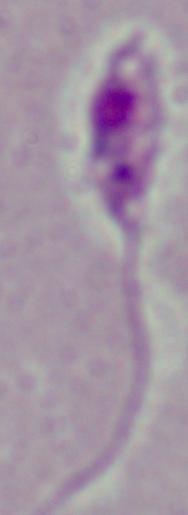

magnification: 1000x
identification: Leishmania
modality: photomicrograph